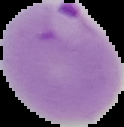

Summary:
  - Malaria status: parasitized
  - Preparation: thin blood film
  - Image type: segmented cell region on a black background
  - Image size: 124×127 pixels